Give the position of every malaria parasite.
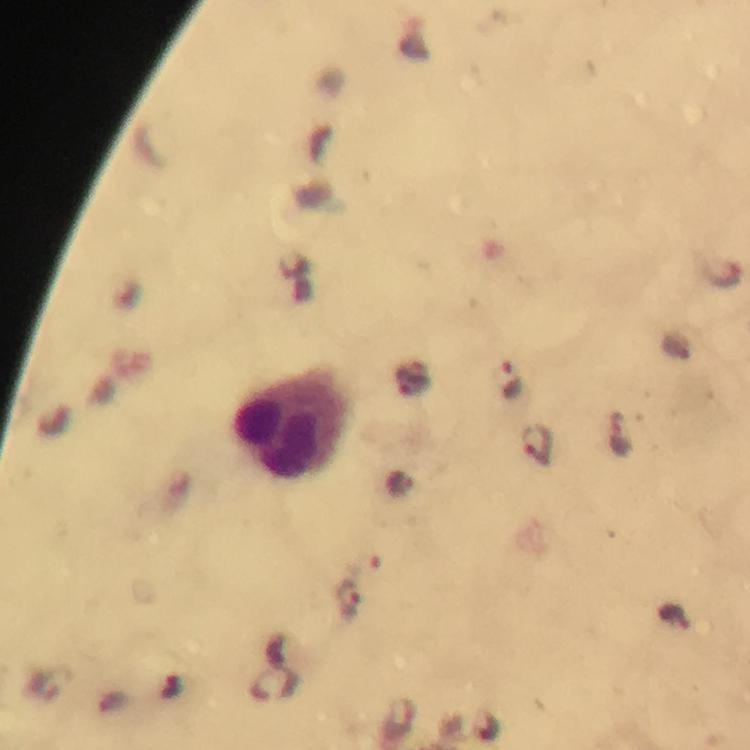
Approximate object centers, in pixels from the top-left corner.
Malaria parasites: (x=722, y=275), (x=411, y=380), (x=511, y=380), (x=620, y=433), (x=537, y=446), (x=402, y=485), (x=348, y=601), (x=675, y=618), (x=489, y=727).

cropped from = one field of view
stain = Giemsa
leukocyte locations = approximate object centers, in pixels from the top-left corner: (x=289, y=426)
capture = smartphone photograph through a microscope
immersion oil = used
image size = 750×750 pixels
magnification = 100x
preparation = thick blood film
context = from a diagnostic examination for malaria